Comment on the morphology of the red blood cells.
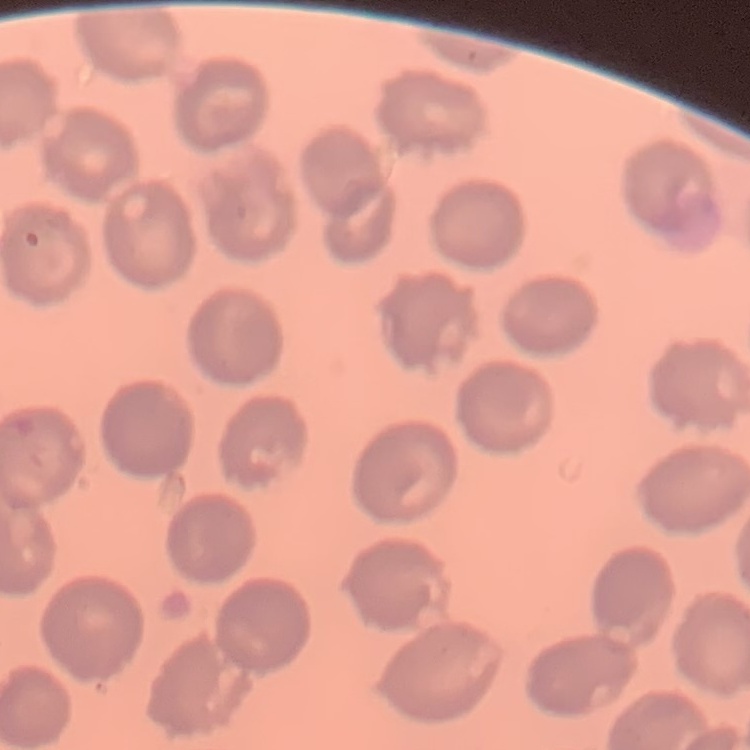

No rouleaux formation.

image type = one tile cut from a larger photomicrograph
stain = Field's or Giemsa
preparation = thin peripheral smear